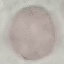

Result: no malaria parasites seen. Photographed with a smartphone camera at the microscope eyepiece. Giemsa-stained preparation. Thin smear of blood. Cell patch, automatically extracted from a larger field of view and resized to 64 × 64 pixels.